Locate every malaria parasite.
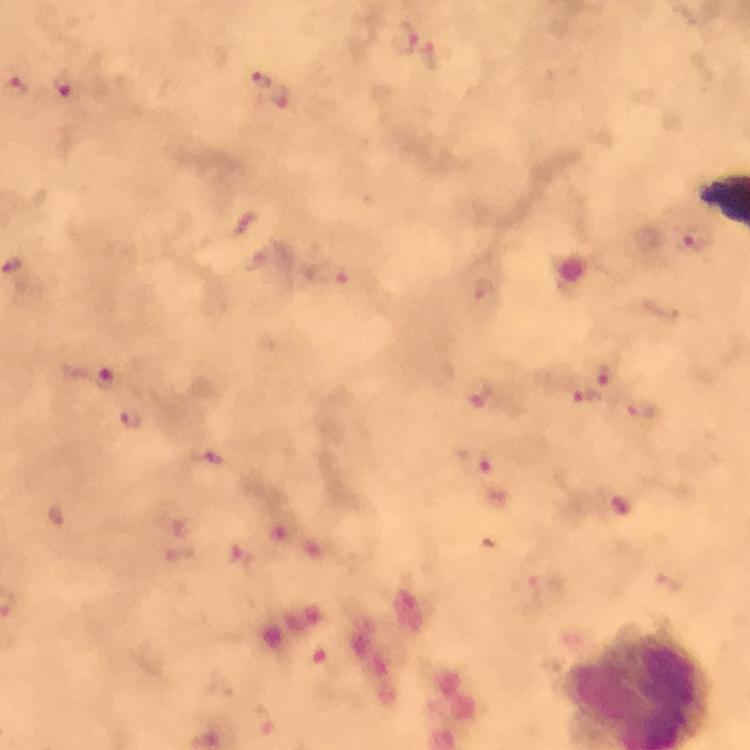
Approximate object centers, in pixels from the top-left corner.
Malaria parasites: (x=403, y=38), (x=261, y=80), (x=64, y=84), (x=697, y=239), (x=604, y=373), (x=482, y=395), (x=588, y=396), (x=640, y=410), (x=477, y=464).

Summary:
  - Context: from a malaria diagnostic workup
  - Preparation: thick blood smear
  - Magnification: 100x
  - Cropped from: one field of view
  - Capture: smartphone mounted on the microscope
  - Image size: 750×750 pixels
  - Immersion oil: applied
  - Stain: Giemsa